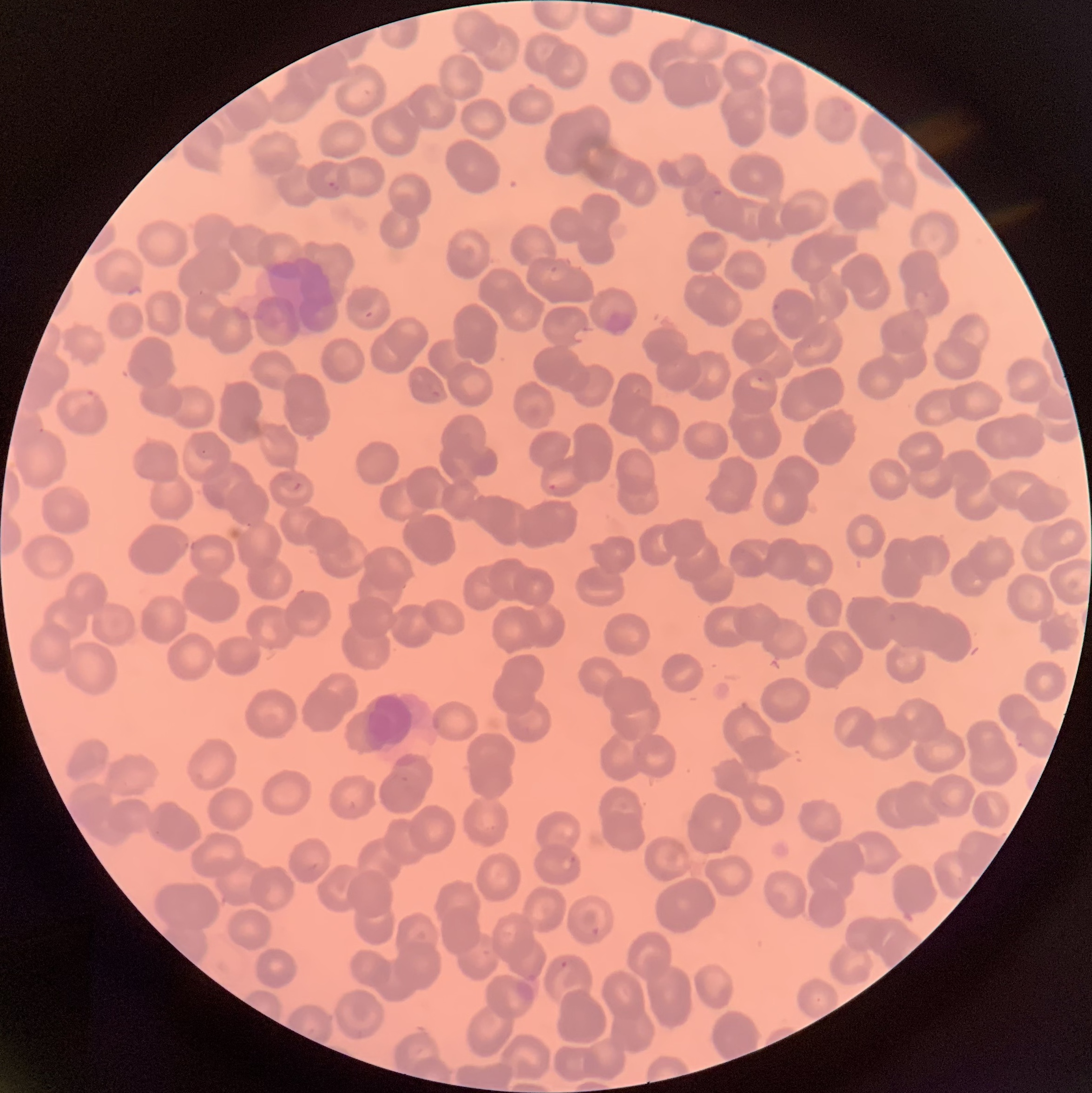
Approximate bounding boxes as named x1/y1/x2/y2 corners in pixels. Plasmodium parasite locations: (x1=327, y1=180, x2=341, y2=192), (x1=711, y1=187, x2=724, y2=199), (x1=363, y1=310, x2=374, y2=321), (x1=79, y1=388, x2=98, y2=406), (x1=431, y1=389, x2=442, y2=399), (x1=199, y1=448, x2=209, y2=457), (x1=291, y1=481, x2=304, y2=492), (x1=546, y1=482, x2=559, y2=492), (x1=562, y1=856, x2=577, y2=871), (x1=590, y1=926, x2=602, y2=938), (x1=559, y1=960, x2=569, y2=969). Thin blood smear. Image is 1092×1093 pixels. The red blood cells show rouleaux formation. Optical microscopy.